Report the malaria status of this cell.
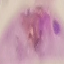
It is parasitized.

Summary:
  - Preparation: thin smear
  - Image type: automatically extracted cell patch, resized to 64 × 64 pixels
  - Stain: Giemsa
  - Capture: smartphone camera at the microscope eyepiece